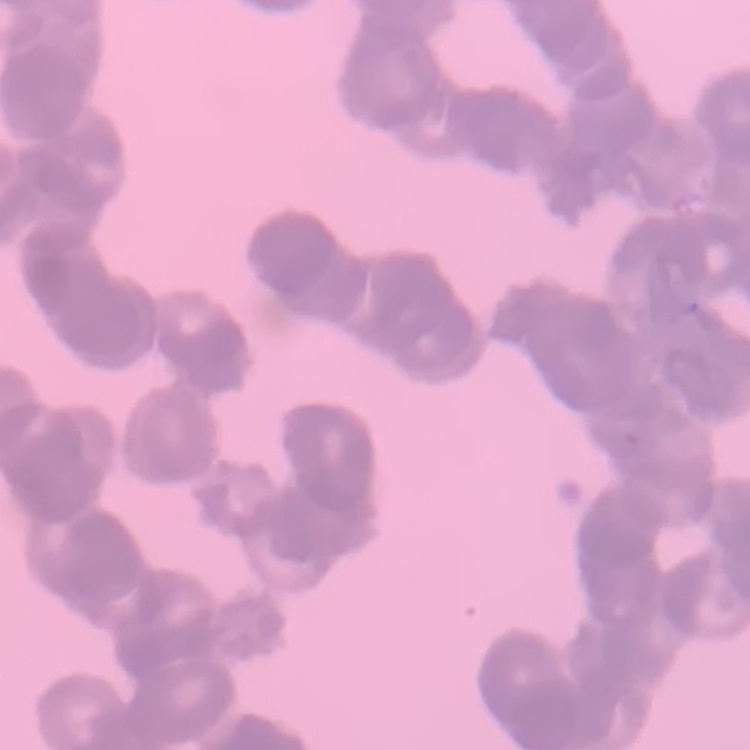
The erythrocytes exhibit rouleaux formation. Stained with either Field's or Giemsa. Thin blood film. Square crop of a larger photomicrograph.